Classify this cell by malaria status.
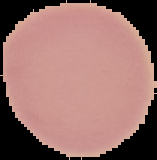
Uninfected.

image size = 157×160 pixels
preparation = thin blood smear
image type = segmented cell region with the area outside set to black